Outline each Plasmodium malariae-infected red blood cell.
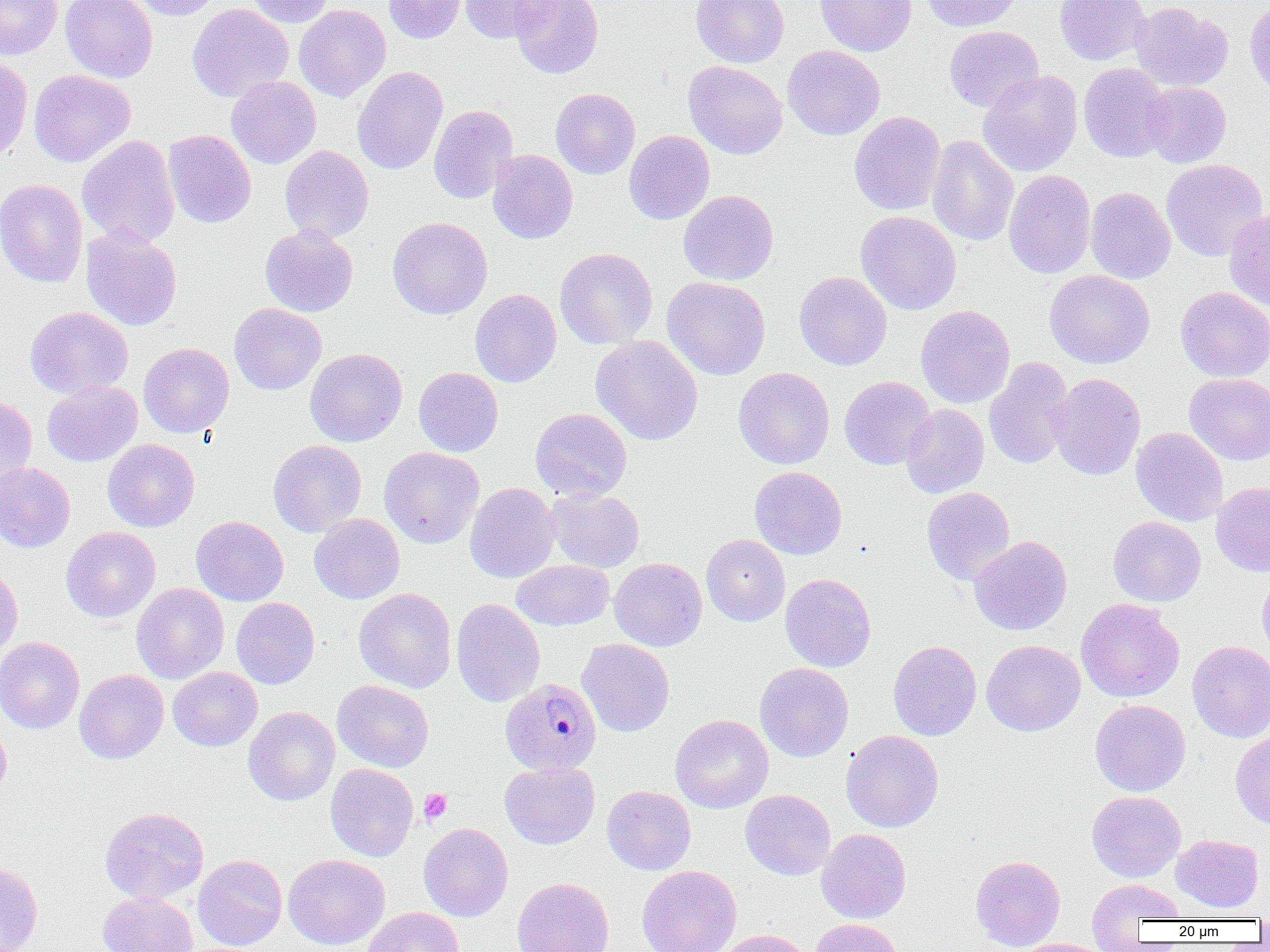

Approximate bounding boxes as (x1, y1, x2, y2) in pixels.
Plasmodium malariae-infected red blood cells: (500, 678, 601, 775).

slide-level diagnosis = Plasmodium malariae
platelet locations = approximate bounding boxes as (x1, y1, x2, y2) in pixels: (419, 789, 452, 824)
preparation = thin blood smear
field of view = one of a larger specimen
magnification = 1000x
image size = 1270×952 pixels
uninfected red blood cell locations = approximate bounding boxes as (x1, y1, x2, y2) in pixels: (0, 0, 62, 59), (60, 0, 158, 82), (126, 0, 224, 20), (246, 0, 335, 27), (383, 0, 467, 43), (459, 0, 561, 44), (509, 0, 604, 79), (691, 0, 789, 67), (815, 0, 917, 56), (922, 0, 1023, 32), (1054, 0, 1149, 65), (1245, 0, 1270, 99), (1130, 1, 1232, 92), (187, 3, 293, 102), (294, 4, 391, 102), (944, 26, 1044, 113), (783, 45, 885, 139), (0, 54, 32, 162), (683, 61, 787, 158), (1078, 62, 1172, 162), (352, 66, 448, 174), (28, 69, 136, 167), (978, 70, 1082, 177), (226, 76, 321, 169), (1141, 82, 1231, 168), (551, 88, 640, 179), (428, 105, 518, 204), (849, 111, 946, 215), (163, 129, 256, 228), (624, 130, 714, 224), (77, 135, 180, 248), (926, 135, 1019, 246), (279, 145, 374, 243), (488, 150, 578, 243), (1161, 159, 1268, 261), (1004, 169, 1095, 278), (0, 178, 88, 288), (1085, 187, 1176, 284), (678, 190, 778, 285), (1224, 208, 1270, 310), (855, 210, 962, 314), (388, 217, 492, 319), (260, 225, 358, 317), (81, 226, 183, 331), (554, 248, 657, 349), (1044, 270, 1154, 368), (794, 271, 892, 370), (662, 276, 770, 379), (1176, 286, 1270, 382), (470, 288, 562, 387), (229, 303, 326, 395), (916, 305, 1015, 408), (25, 306, 133, 398), (591, 335, 703, 446), (138, 342, 234, 437), (305, 348, 407, 446), (984, 357, 1075, 470), (414, 367, 503, 457), (734, 367, 835, 469), (1049, 373, 1146, 480), (1185, 373, 1270, 465), (839, 376, 936, 469), (42, 381, 142, 466), (0, 395, 37, 490), (900, 404, 989, 498), (530, 407, 632, 501), (1130, 426, 1228, 526), (102, 439, 200, 531), (268, 439, 366, 536), (379, 447, 484, 548), (0, 463, 75, 552), (749, 466, 847, 559), (1211, 481, 1270, 577), (464, 482, 560, 583), (922, 486, 1015, 586), (546, 488, 644, 572), (309, 514, 405, 604), (191, 516, 288, 606), (1108, 516, 1206, 606), (60, 526, 160, 622), (701, 534, 790, 626), (969, 536, 1072, 635), (609, 557, 707, 651), (512, 559, 614, 630), (0, 565, 22, 659), (1257, 572, 1270, 666), (780, 573, 876, 672), (131, 583, 229, 684), (354, 588, 456, 693), (231, 597, 320, 689), (451, 598, 546, 707), (1076, 598, 1184, 703), (0, 637, 85, 733), (577, 638, 675, 737), (981, 639, 1085, 736), (888, 640, 982, 741), (1187, 640, 1270, 742), (755, 663, 853, 761), (168, 667, 263, 751), (74, 669, 168, 763), (332, 680, 434, 772), (1090, 699, 1190, 796), (243, 706, 340, 806), (670, 714, 773, 813), (0, 719, 12, 802), (840, 730, 944, 832), (1230, 731, 1270, 829), (500, 761, 600, 849), (325, 763, 418, 862), (601, 785, 696, 875), (740, 789, 835, 880), (1087, 791, 1185, 882), (100, 807, 209, 904), (418, 823, 513, 921), (816, 829, 911, 923), (1171, 834, 1264, 912), (283, 853, 390, 950), (193, 854, 287, 950), (970, 855, 1065, 950), (0, 861, 43, 952), (637, 865, 741, 952), (512, 876, 614, 952), (1087, 877, 1185, 936), (97, 892, 198, 952), (363, 906, 464, 952), (811, 918, 903, 952), (714, 929, 813, 952), (1015, 938, 1112, 952)
modality = light microscopy